Comment on the morphology of the red blood cells.
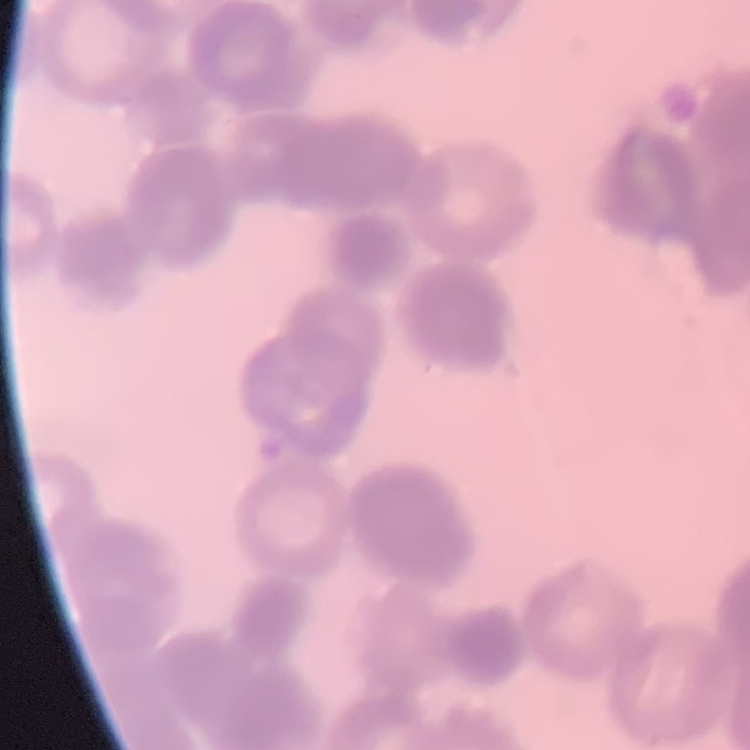

They show rouleaux formation.

stain: Field's or Giemsa
preparation: thin peripheral smear
image_type: square crop of a larger photomicrograph